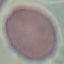
Summary:
  - Result: no malaria parasites seen
  - Preparation: thin smear
  - Capture: smartphone through the microscope eyepiece
  - Image type: cell patch, automatically extracted from a larger field of view and resized to 64 × 64 pixels
  - Stain: Giemsa